Locate and identify every blood parasite.
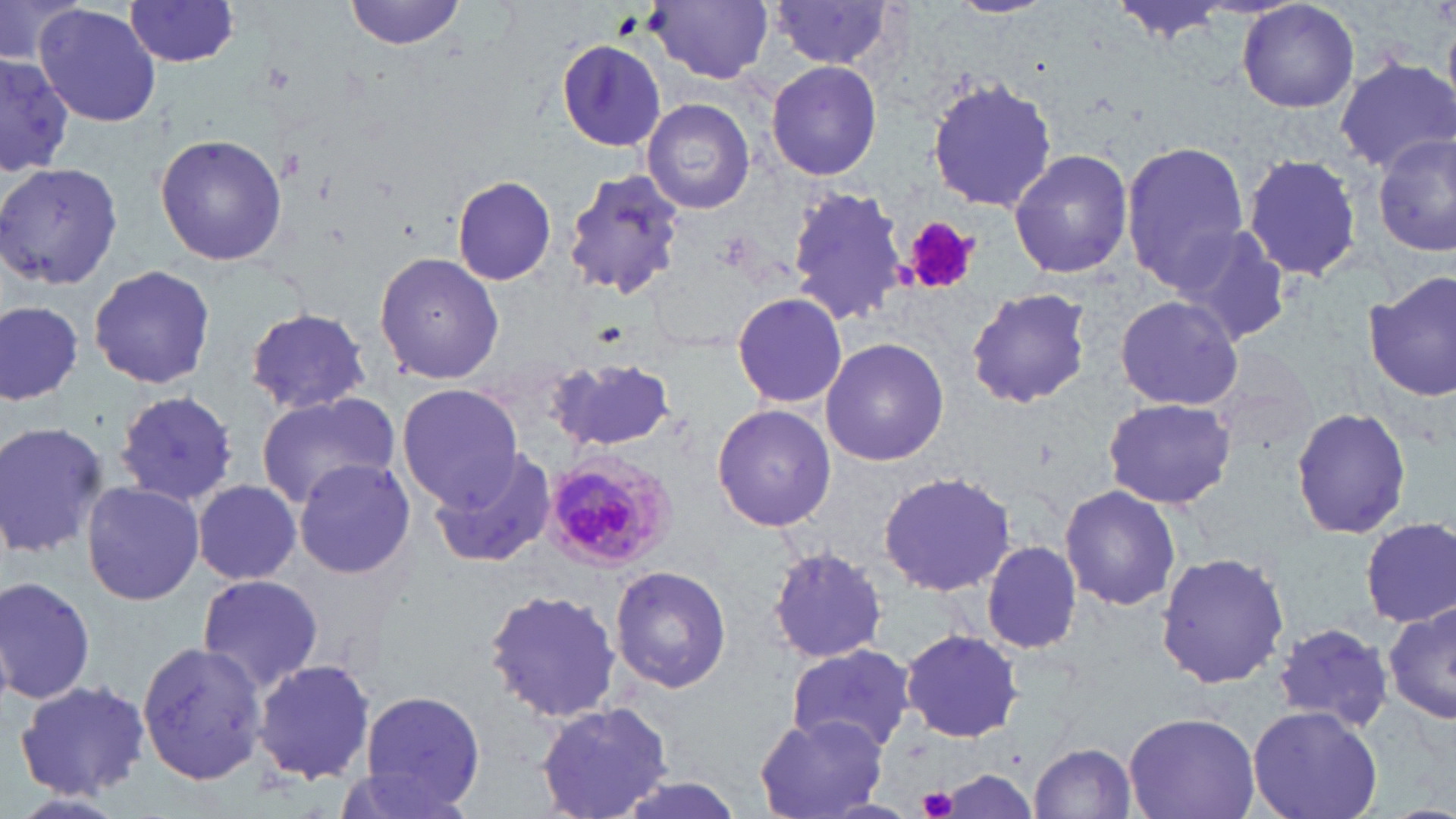
Approximate bounding boxes as named x1/y1/x2/y2 corners in pixels.
Plasmodium malariae-infected red blood cells: (x1=541, y1=450, x2=680, y2=575).
No Plasmodium falciparum, Plasmodium ovale, Plasmodium vivax, Babesia divergens, or Trypanosoma brucei observed.

Summary:
  - Uninfected red blood cell locations: (x1=0, y1=0, x2=84, y2=67), (x1=342, y1=0, x2=471, y2=52), (x1=1114, y1=0, x2=1234, y2=43), (x1=1238, y1=0, x2=1361, y2=114), (x1=124, y1=1, x2=243, y2=68), (x1=649, y1=1, x2=773, y2=84), (x1=768, y1=2, x2=903, y2=72), (x1=35, y1=4, x2=161, y2=128), (x1=556, y1=39, x2=666, y2=149), (x1=0, y1=55, x2=79, y2=173), (x1=767, y1=59, x2=883, y2=181), (x1=1336, y1=60, x2=1455, y2=171), (x1=926, y1=76, x2=1060, y2=214), (x1=643, y1=99, x2=753, y2=215), (x1=154, y1=133, x2=289, y2=267), (x1=1372, y1=133, x2=1456, y2=259), (x1=1120, y1=141, x2=1249, y2=289), (x1=1008, y1=148, x2=1135, y2=281), (x1=1242, y1=153, x2=1363, y2=282), (x1=0, y1=162, x2=123, y2=291), (x1=561, y1=168, x2=688, y2=301), (x1=452, y1=175, x2=556, y2=286), (x1=784, y1=185, x2=908, y2=324), (x1=1171, y1=221, x2=1296, y2=346), (x1=374, y1=250, x2=506, y2=385), (x1=88, y1=264, x2=218, y2=391), (x1=1364, y1=273, x2=1456, y2=402), (x1=965, y1=286, x2=1095, y2=409), (x1=731, y1=291, x2=847, y2=410), (x1=1113, y1=295, x2=1243, y2=411), (x1=0, y1=301, x2=82, y2=408), (x1=244, y1=307, x2=370, y2=415), (x1=819, y1=336, x2=950, y2=466), (x1=549, y1=359, x2=680, y2=452), (x1=397, y1=383, x2=522, y2=507), (x1=113, y1=391, x2=237, y2=507), (x1=254, y1=391, x2=401, y2=508), (x1=1102, y1=396, x2=1238, y2=510), (x1=712, y1=404, x2=837, y2=533), (x1=1290, y1=406, x2=1414, y2=540), (x1=0, y1=420, x2=109, y2=560), (x1=428, y1=448, x2=559, y2=570), (x1=291, y1=458, x2=418, y2=579), (x1=879, y1=470, x2=1018, y2=598), (x1=192, y1=479, x2=305, y2=587), (x1=80, y1=480, x2=205, y2=607), (x1=1058, y1=483, x2=1181, y2=611), (x1=1361, y1=517, x2=1455, y2=630), (x1=980, y1=538, x2=1084, y2=655), (x1=769, y1=546, x2=888, y2=664), (x1=1155, y1=550, x2=1291, y2=690), (x1=610, y1=564, x2=734, y2=693), (x1=194, y1=573, x2=326, y2=695), (x1=0, y1=574, x2=97, y2=707), (x1=483, y1=589, x2=625, y2=724), (x1=1382, y1=602, x2=1456, y2=728), (x1=1272, y1=622, x2=1392, y2=730), (x1=901, y1=629, x2=1025, y2=743), (x1=136, y1=639, x2=267, y2=788), (x1=784, y1=644, x2=917, y2=753), (x1=252, y1=660, x2=376, y2=787), (x1=15, y1=679, x2=153, y2=798), (x1=359, y1=690, x2=488, y2=810), (x1=533, y1=701, x2=676, y2=819), (x1=1246, y1=706, x2=1384, y2=819), (x1=1122, y1=710, x2=1261, y2=819), (x1=755, y1=713, x2=889, y2=818), (x1=1029, y1=741, x2=1139, y2=819), (x1=602, y1=772, x2=751, y2=819), (x1=10, y1=790, x2=131, y2=819)
  - Platelet locations: (x1=906, y1=217, x2=978, y2=296), (x1=918, y1=786, x2=959, y2=817)
  - Slide-level diagnosis: Plasmodium malariae
  - Stain: May-Grünwald-Giemsa
  - Modality: light microscopy
  - Image size: 1456×819 pixels
  - Preparation: thin blood smear
  - Field of view: single
  - Magnification: 1000x